State which cell type is depicted.
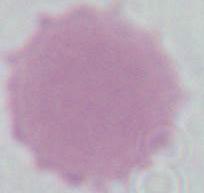
An erythrocyte.

Micrograph. 1000x magnification.